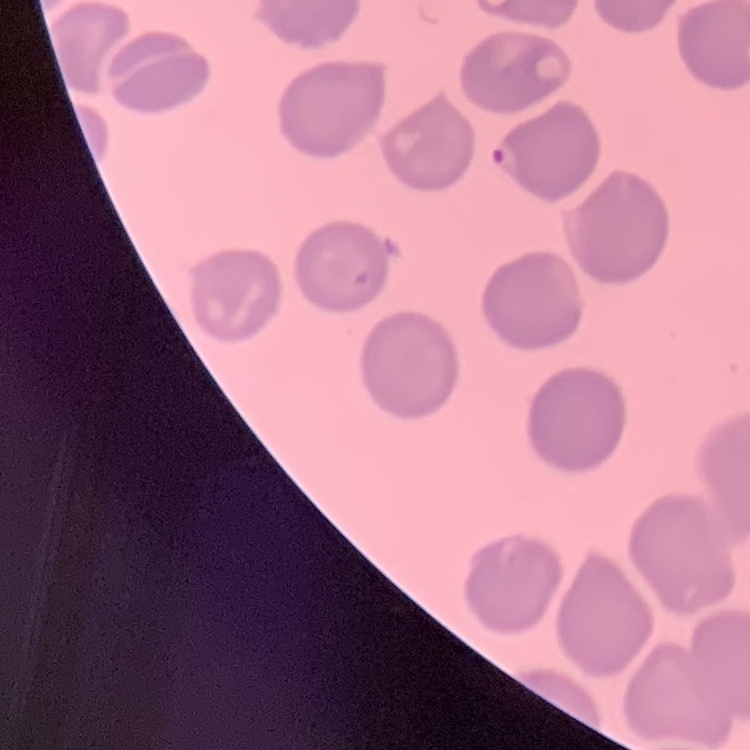
red blood cell morphology = no rouleaux formation
stain = Field's or Giemsa
image type = one tile cut from a larger photomicrograph
preparation = thin peripheral smear